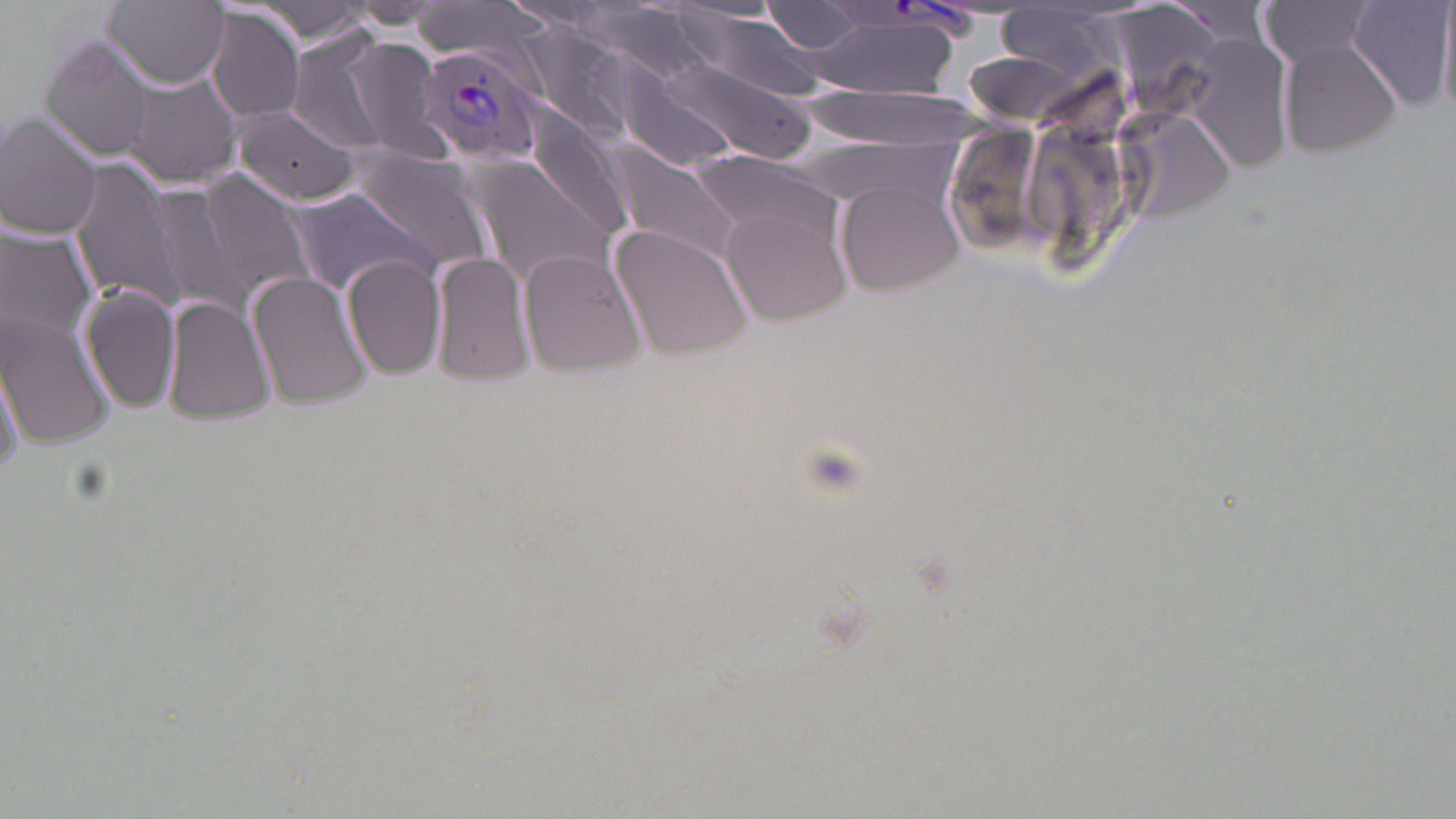 Approximate bounding boxes as (x1,y1)-(x2,y2) corner pairs in pixels. Plasmodium vivax-infected red blood cell locations: (416,43)-(549,164). Uninfected red blood cell locations: (103,0)-(228,89), (413,1)-(551,60), (761,1)-(873,55), (1257,1)-(1383,66), (251,2)-(377,44), (1347,2)-(1455,109), (337,4)-(445,31), (576,4)-(714,87), (669,4)-(804,32), (993,6)-(1128,80), (206,8)-(307,124), (684,13)-(822,100), (805,16)-(962,98), (523,27)-(628,130), (1185,34)-(1294,176), (41,35)-(153,162), (342,38)-(452,160), (1279,38)-(1404,157), (290,39)-(389,153), (662,57)-(814,163), (615,71)-(743,175), (124,73)-(240,186), (795,86)-(983,145), (233,104)-(358,205), (1116,110)-(1239,223), (0,111)-(103,239), (526,113)-(637,245), (605,143)-(745,267), (348,145)-(492,273), (694,151)-(853,256), (463,152)-(617,292), (70,161)-(184,308), (193,171)-(317,304), (838,182)-(966,296), (145,186)-(236,305), (289,188)-(434,294), (717,200)-(853,329), (611,223)-(752,361), (0,225)-(98,347), (430,249)-(536,390), (519,249)-(648,378), (343,254)-(446,382), (247,269)-(372,412), (79,286)-(181,413), (162,296)-(275,427), (1,311)-(115,450), (1,346)-(27,486). Slide-level diagnosis: Plasmodium vivax. Optical microscopy. May-Grünwald-Giemsa stain. Thin blood smear. Single field of view. Image is 1456×819 pixels. 1000x magnification.